Describe the morphology of the red blood cells.
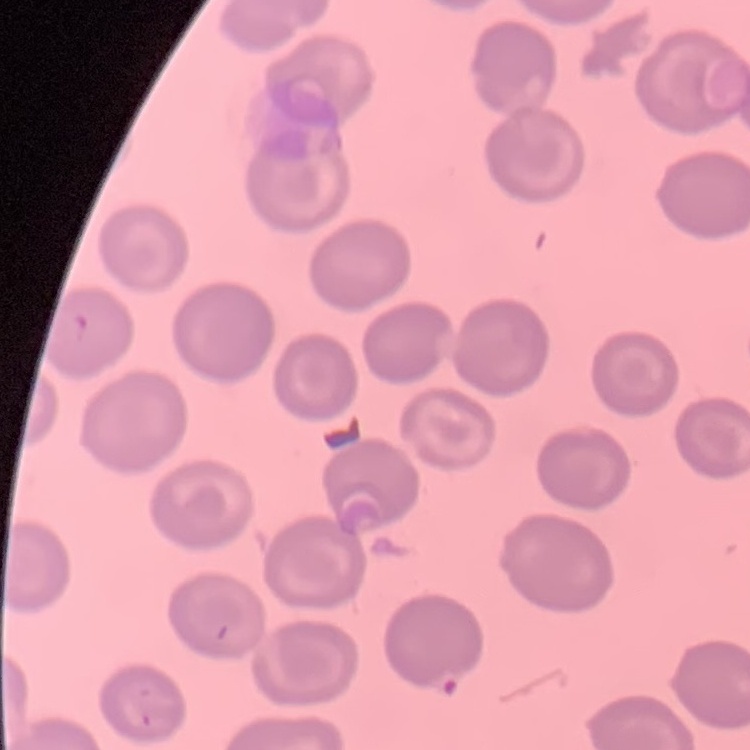

No rouleaux formation.

Thin blood film. Square crop of a larger photomicrograph. Stained with either Field's or Giemsa.